Give the position of every malaria parasite.
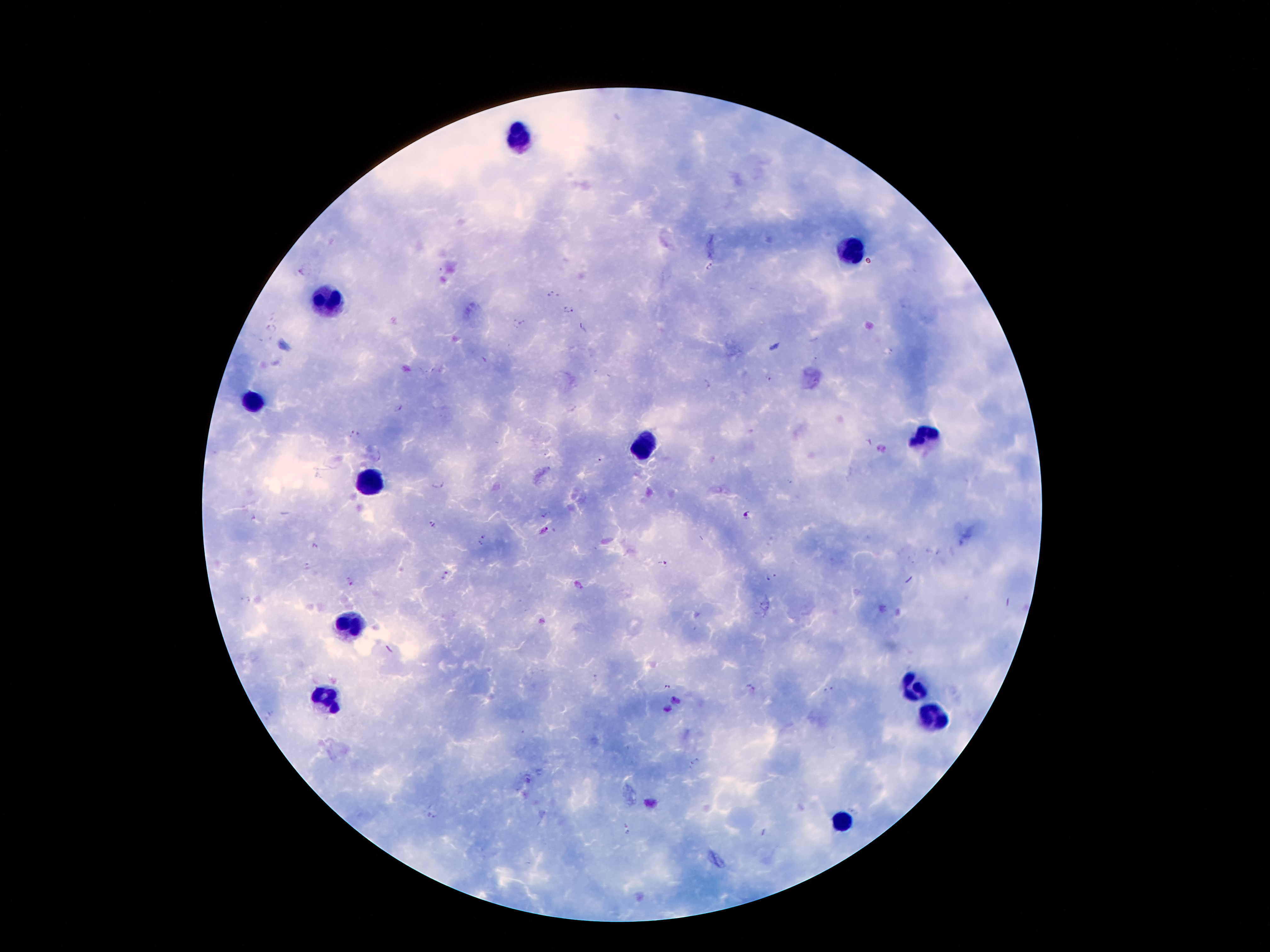
Approximate centers as (x, y) in pixels.
Malaria parasites: (710, 265), (302, 271), (551, 295), (567, 307), (518, 322), (271, 324), (583, 330), (483, 360), (767, 380), (705, 387), (398, 408), (355, 433), (598, 459), (438, 485), (745, 514), (546, 515), (255, 518), (434, 524), (543, 531), (481, 539), (315, 545), (309, 564), (663, 564), (446, 574), (769, 578), (349, 581), (594, 678), (667, 687), (828, 687), (750, 690), (675, 700), (666, 709), (695, 762), (437, 816), (627, 831), (764, 832).

{
  "image_size": "1270×952 pixels",
  "capture": "smartphone camera through the microscope eyepiece",
  "preparation": "thick blood film",
  "magnification": "100x",
  "stain": "Giemsa",
  "patient_malaria_status": "infected with Plasmodium falciparum",
  "field_of_view": "single",
  "leukocyte_locations": "approximate centers as (x, y) in pixels: (522, 132), (851, 253), (320, 305), (253, 403), (923, 436), (646, 445), (369, 485), (354, 623), (910, 685), (327, 700), (928, 717), (841, 821)"
}